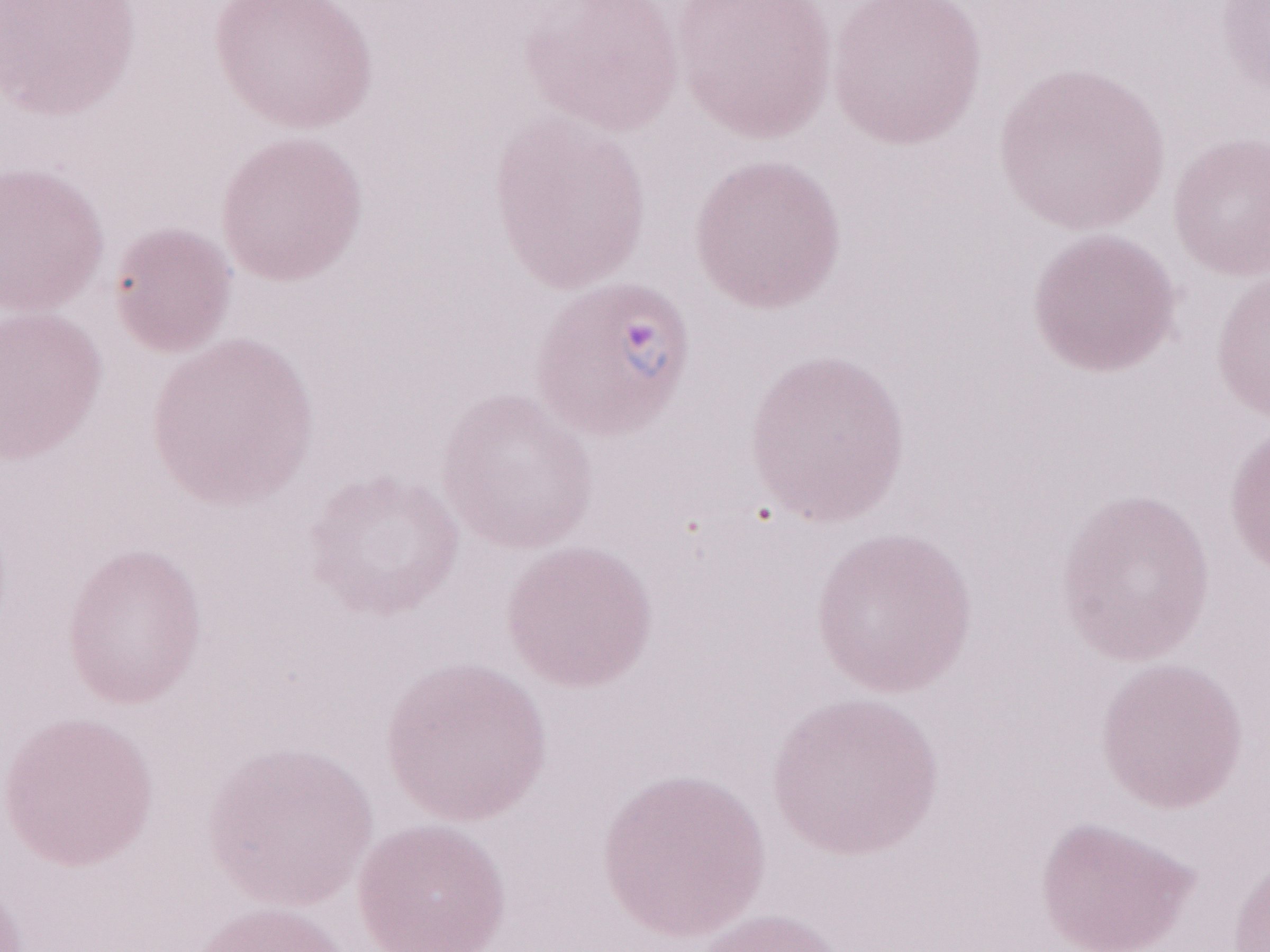

1,000x magnification. Image is 1270×952 pixels. Single field of view. Patient diagnosis: malaria infection. Olympus BX43 microscope and DP73 digital camera. Thin blood smear. May-Grünwald-Giemsa-stained preparation.